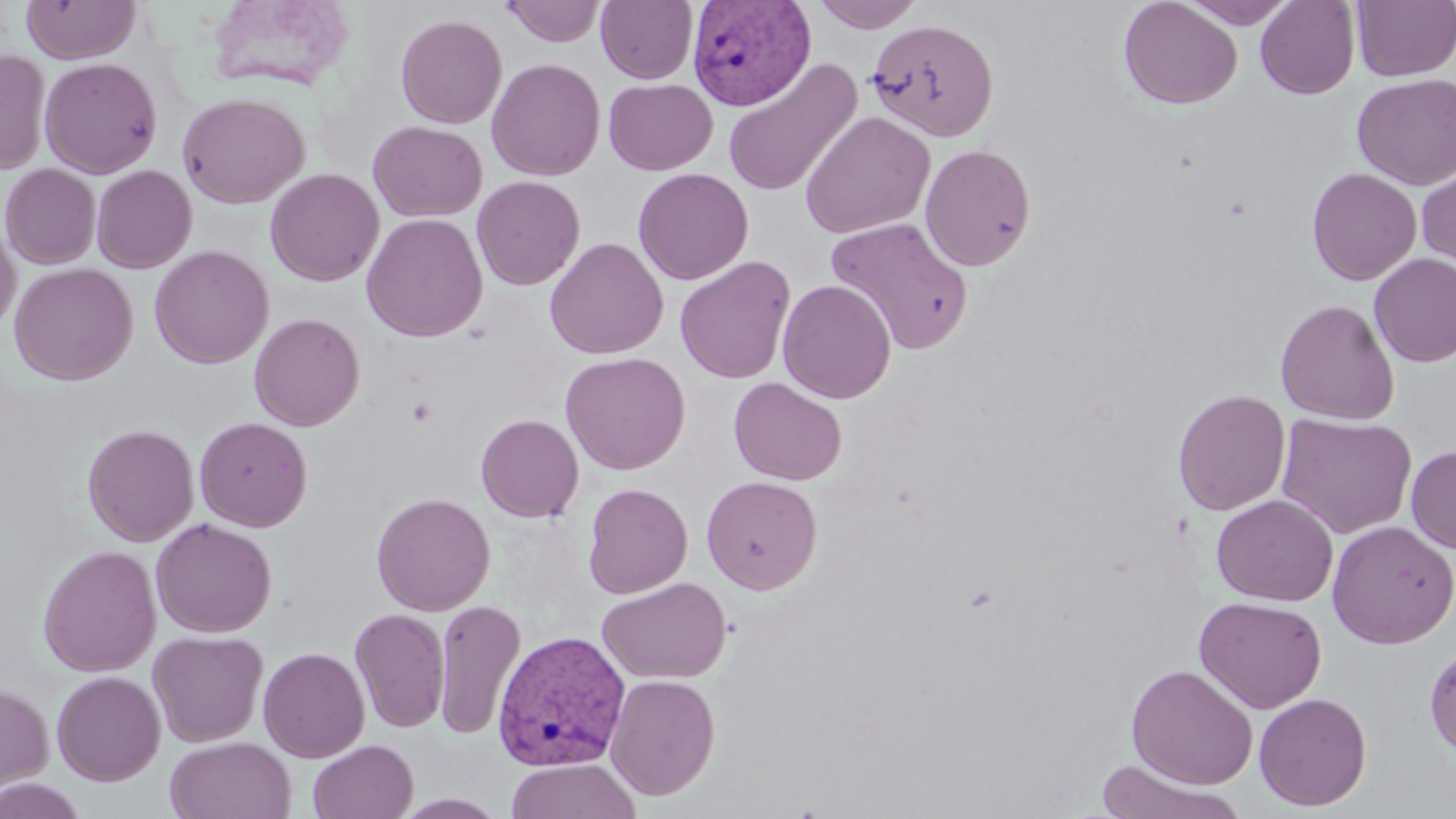
Approximate bounding boxes as [x1, y1, x2, y2] in pixels. Uninfected red blood cell locations: [21, 0, 139, 64], [203, 0, 357, 94], [810, 0, 928, 32], [1118, 0, 1243, 110], [1181, 0, 1297, 28], [501, 1, 607, 46], [596, 1, 698, 84], [1255, 1, 1360, 99], [1351, 1, 1456, 82], [395, 14, 507, 129], [866, 17, 999, 142], [0, 49, 51, 175], [40, 57, 162, 179], [722, 57, 862, 199], [486, 58, 606, 180], [1352, 74, 1456, 189], [603, 78, 718, 175], [177, 91, 310, 208], [800, 110, 936, 239], [368, 120, 487, 221], [920, 143, 1036, 271], [1416, 155, 1456, 274], [0, 163, 101, 269], [91, 165, 197, 273], [633, 167, 754, 285], [1307, 167, 1422, 286], [265, 168, 384, 286], [471, 175, 585, 291], [361, 213, 488, 342], [825, 216, 974, 354], [0, 224, 20, 332], [544, 237, 668, 360], [150, 245, 274, 369], [1369, 253, 1456, 367], [674, 256, 796, 384], [9, 263, 138, 385], [777, 279, 896, 403], [1275, 299, 1400, 425], [249, 312, 365, 431], [560, 351, 691, 475], [729, 378, 847, 485], [1172, 389, 1290, 515], [1276, 412, 1418, 539], [476, 413, 584, 522], [194, 416, 312, 532], [82, 423, 200, 546], [1406, 445, 1456, 554], [701, 475, 822, 595], [582, 482, 693, 599], [371, 491, 495, 616], [1211, 494, 1338, 607], [150, 518, 277, 637], [1327, 520, 1456, 648], [38, 544, 161, 677], [597, 576, 732, 685], [1195, 595, 1327, 713], [434, 599, 525, 740], [349, 608, 450, 733], [148, 630, 268, 747], [1424, 642, 1456, 761], [258, 646, 370, 763], [1126, 663, 1258, 790], [51, 670, 166, 785], [604, 673, 721, 800], [0, 680, 54, 795], [1253, 691, 1373, 811], [165, 736, 297, 819], [308, 739, 419, 819], [505, 757, 641, 819], [1093, 759, 1248, 819], [0, 777, 89, 819], [391, 792, 510, 819]. Platelet locations: [406, 396, 437, 426]. Plasmodium vivax-infected red blood cell locations: [687, 1, 815, 111], [492, 630, 631, 771]. Slide-level diagnosis: Plasmodium vivax. Thin blood film. Image is 1456×819 pixels. Single field of view. Optical microscopy. May-Grünwald-Giemsa stain. Captured at 1000x magnification.